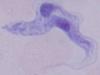

identification = trypanosome
modality = photomicrograph
magnification = 1000x